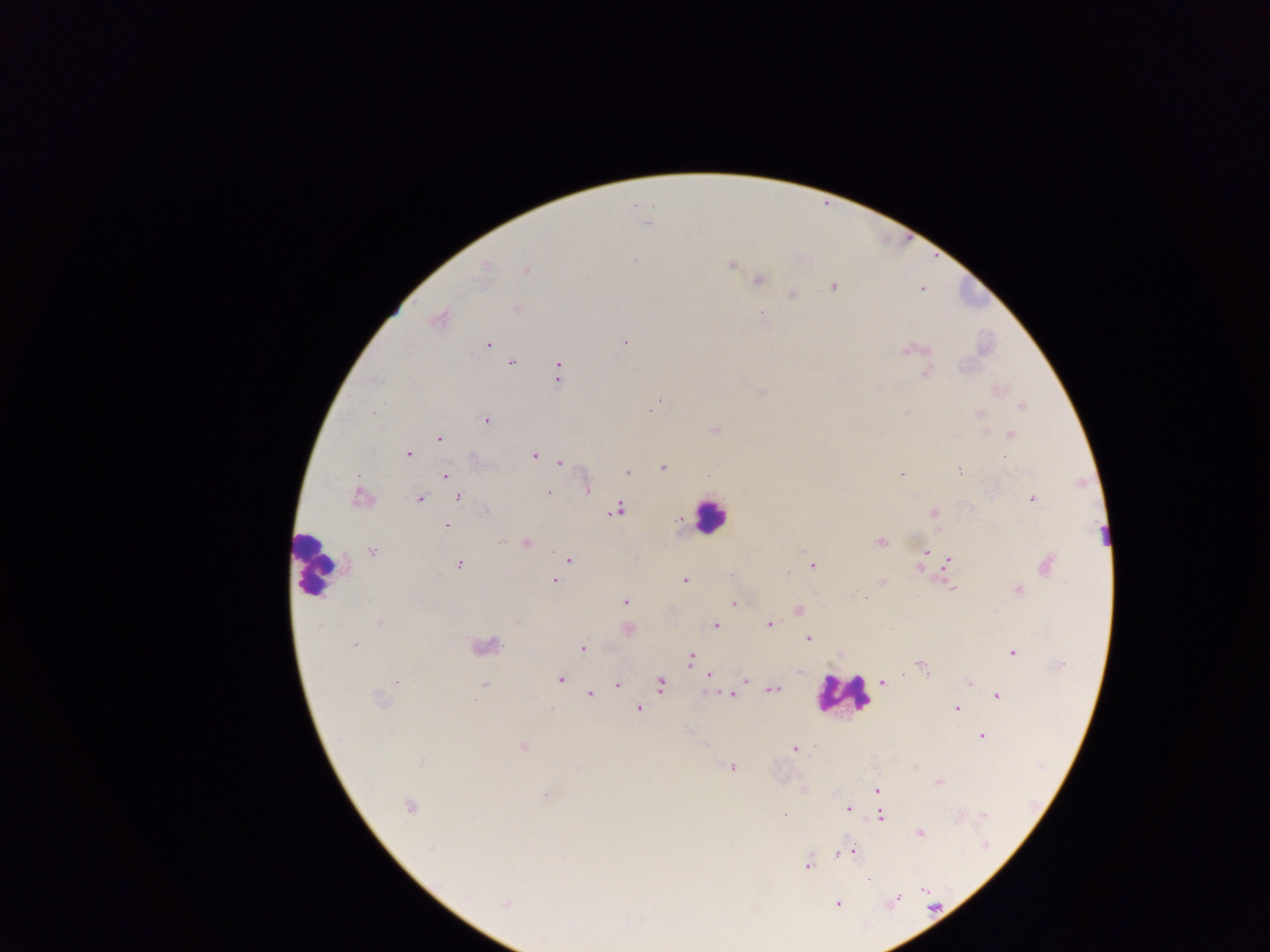

Approximate centers as (x, y) in pixels.
Summary:
  - Leukocyte locations: (711, 514), (315, 565), (484, 649), (844, 694)
  - Plasmodium parasite locations: (647, 223), (635, 261), (732, 264), (485, 269), (526, 271), (759, 279), (834, 287), (922, 289), (792, 294), (517, 308), (762, 312), (438, 319), (625, 342), (487, 345), (907, 351), (512, 363), (926, 373), (558, 374), (1021, 406), (652, 408), (373, 413), (907, 413), (980, 413), (485, 420), (715, 430), (1012, 435), (439, 437), (408, 454), (534, 456), (1005, 458), (561, 463), (663, 467), (959, 471), (627, 472), (902, 474), (445, 476), (586, 488), (548, 492), (359, 497), (458, 497), (419, 499), (1032, 499), (617, 510), (485, 511), (933, 513), (446, 525), (880, 541), (503, 542), (527, 543), (372, 551), (926, 552), (923, 558), (568, 560), (948, 561), (1048, 564), (459, 565), (812, 565), (917, 568), (788, 572), (554, 580), (684, 580), (882, 581), (953, 588), (1018, 590), (865, 598), (625, 601), (733, 604), (798, 611), (380, 623), (319, 625), (769, 625), (715, 626), (628, 630), (808, 638), (354, 644), (583, 648), (1013, 653), (691, 658), (1061, 665), (923, 668), (709, 676), (560, 679), (746, 681), (882, 682), (970, 682), (397, 683), (484, 684), (617, 685), (661, 685), (774, 689), (590, 694), (731, 695), (998, 696), (379, 700), (956, 708), (638, 709), (982, 736), (523, 747), (795, 749), (421, 762), (732, 767), (939, 782), (877, 790), (546, 795), (408, 806), (848, 809), (784, 815), (880, 816), (919, 833), (430, 848), (849, 851), (837, 853), (808, 865), (868, 880), (924, 890), (896, 899), (506, 904), (838, 904)
  - Field of view: single
  - Preparation: thick blood film
  - Image size: 1270×952 pixels
  - Capture: mobile-phone photograph through a microscope
  - Country: Ghana